Point out each malaria parasite.
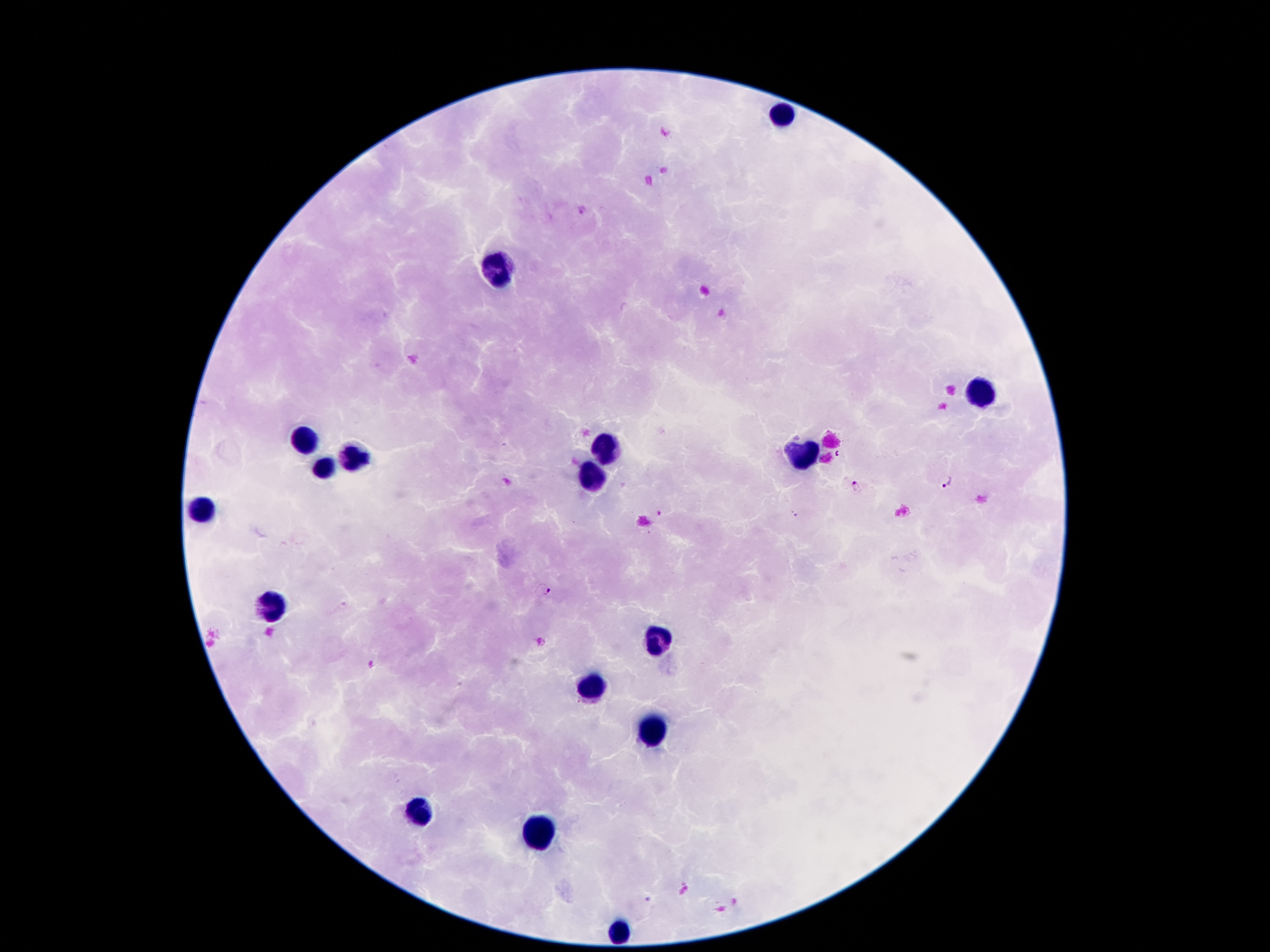
Approximate centers as [x, y] in pixels.
Malaria parasites: [946, 483], [857, 488], [542, 588], [539, 642].

leukocyte locations = [783, 114], [500, 276], [983, 393], [302, 441], [605, 448], [806, 452], [355, 454], [323, 469], [592, 479], [204, 511], [273, 609], [657, 643], [592, 687], [653, 731], [414, 815], [540, 834], [620, 931]
image size = 1270×952 pixels
field of view = single
capture = smartphone through the microscope eyepiece
preparation = thick blood film
patient malaria status = positive for Plasmodium falciparum
magnification = 100x
stain = Giemsa